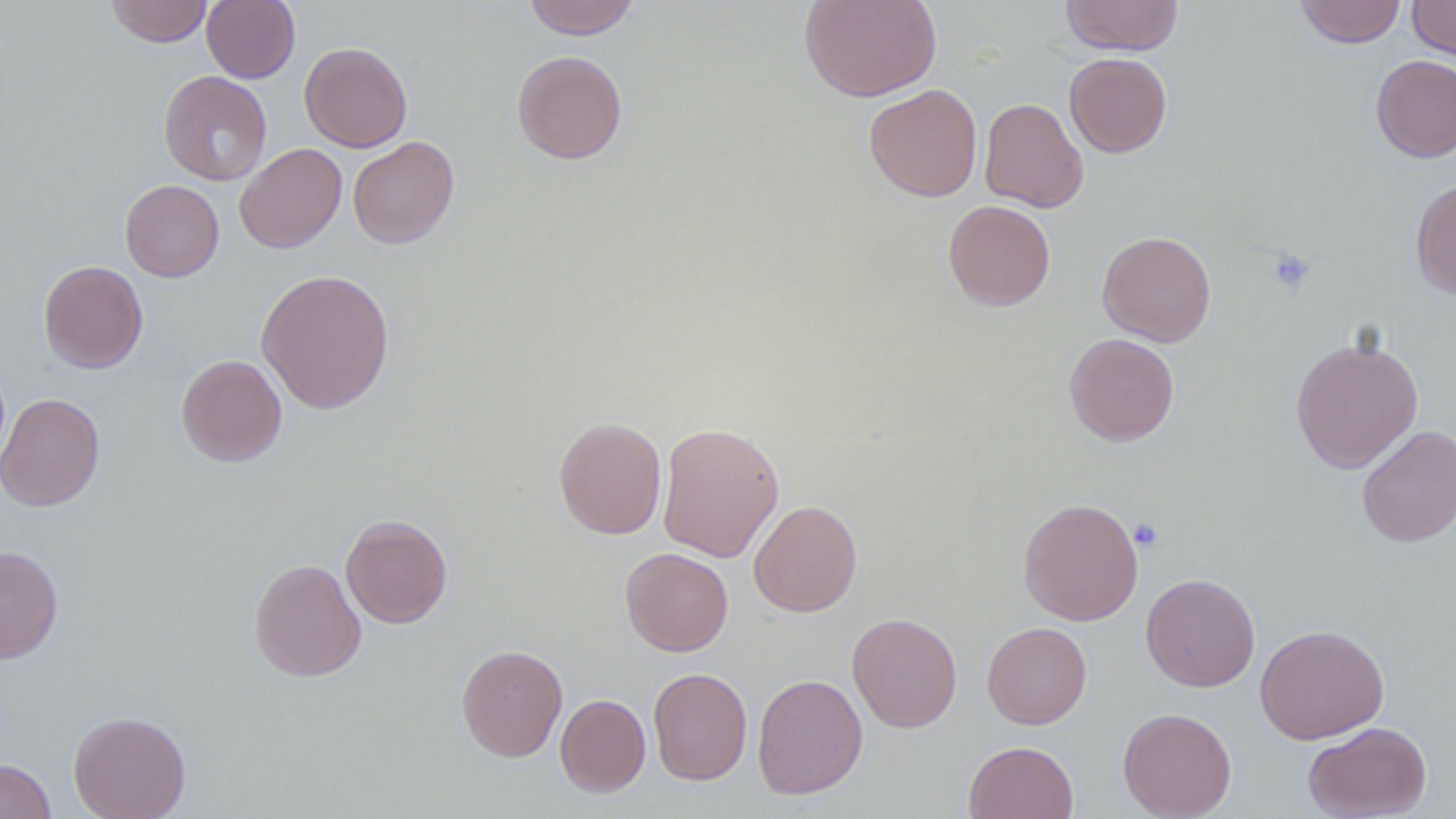

{
  "slide_level_diagnosis": "no evidence of blood parasites",
  "image_size": "1456×819 pixels",
  "modality": "light microscopy",
  "uninfected_red_blood_cell_locations": "approximate bounding boxes as named x1/y1/x2/y2 corners in pixels: (x1=105, y1=0, x2=213, y2=47), (x1=522, y1=0, x2=641, y2=39), (x1=799, y1=0, x2=942, y2=102), (x1=1060, y1=0, x2=1184, y2=56), (x1=1295, y1=0, x2=1406, y2=48), (x1=1407, y1=0, x2=1456, y2=61), (x1=202, y1=1, x2=300, y2=83), (x1=299, y1=42, x2=413, y2=152), (x1=512, y1=50, x2=628, y2=165), (x1=1065, y1=52, x2=1172, y2=157), (x1=1371, y1=55, x2=1456, y2=163), (x1=159, y1=71, x2=272, y2=186), (x1=863, y1=84, x2=983, y2=202), (x1=979, y1=97, x2=1088, y2=213), (x1=347, y1=136, x2=460, y2=249), (x1=234, y1=143, x2=347, y2=253), (x1=1410, y1=177, x2=1456, y2=299), (x1=120, y1=179, x2=224, y2=281), (x1=943, y1=199, x2=1056, y2=311), (x1=1097, y1=230, x2=1216, y2=346), (x1=38, y1=260, x2=148, y2=373), (x1=256, y1=268, x2=395, y2=414), (x1=1064, y1=333, x2=1179, y2=446), (x1=1290, y1=335, x2=1423, y2=473), (x1=176, y1=354, x2=287, y2=467), (x1=0, y1=392, x2=104, y2=512), (x1=553, y1=415, x2=667, y2=540), (x1=657, y1=421, x2=784, y2=563), (x1=1357, y1=424, x2=1455, y2=547), (x1=1018, y1=497, x2=1143, y2=626), (x1=749, y1=500, x2=862, y2=617), (x1=340, y1=514, x2=453, y2=628), (x1=0, y1=545, x2=63, y2=663), (x1=620, y1=547, x2=733, y2=656), (x1=249, y1=558, x2=367, y2=681), (x1=1140, y1=573, x2=1260, y2=692), (x1=846, y1=612, x2=963, y2=733), (x1=981, y1=622, x2=1091, y2=729), (x1=1254, y1=623, x2=1389, y2=744), (x1=456, y1=644, x2=567, y2=761), (x1=648, y1=667, x2=752, y2=785), (x1=752, y1=673, x2=868, y2=800), (x1=555, y1=694, x2=650, y2=797), (x1=1117, y1=708, x2=1237, y2=818), (x1=68, y1=710, x2=191, y2=819), (x1=1303, y1=721, x2=1432, y2=819), (x1=964, y1=741, x2=1079, y2=819), (x1=0, y1=759, x2=56, y2=819)",
  "preparation": "thin blood smear",
  "platelet_locations": "approximate bounding boxes as named x1/y1/x2/y2 corners in pixels: (x1=1267, y1=248, x2=1315, y2=293), (x1=1129, y1=518, x2=1164, y2=551)",
  "field_of_view": "one of a larger specimen",
  "magnification": "1000x"
}